Assess this cell for malaria.
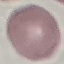
Uninfected.

Acquired by smartphone through the microscope eyepiece. Giemsa-stained preparation. Cell patch, automatically extracted from a larger field of view and resized to 64 × 64 pixels. Thin smear of blood.